Report the malaria status of this cell.
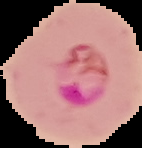

Parasitized.

Summary:
  - Image size: 142×148 pixels
  - Preparation: thin blood film
  - Image type: segmented cell region on a black background